Locate every Plasmodium parasite.
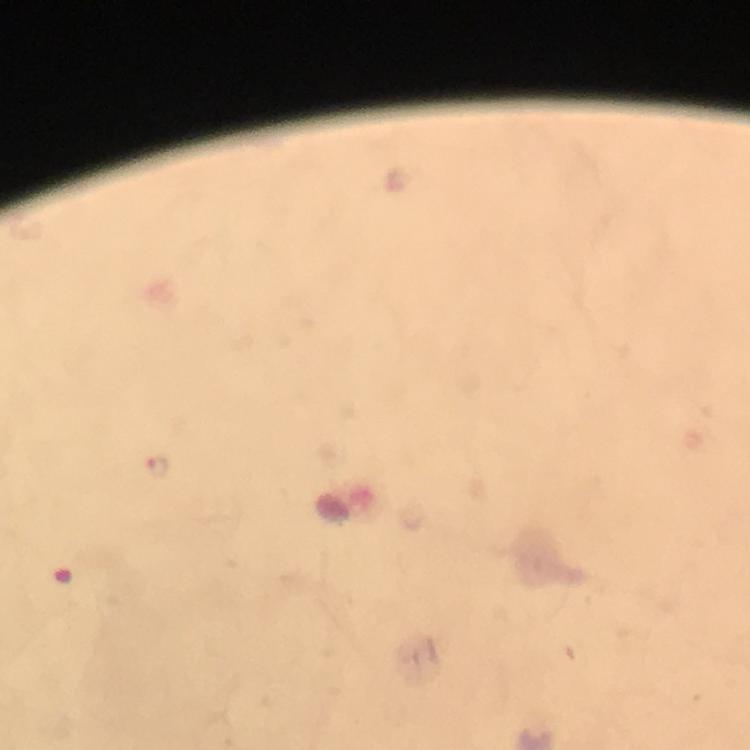

Approximate object centers, in pixels from the top-left corner.
Plasmodium parasites: (x=158, y=467).

preparation: thick blood film
capture: smartphone camera through the microscope
image_size: 750×750 pixels
immersion_oil: applied
cropped_from: a single field of view
context: from a malaria diagnostic workup
magnification: 100x
stain: Giemsa